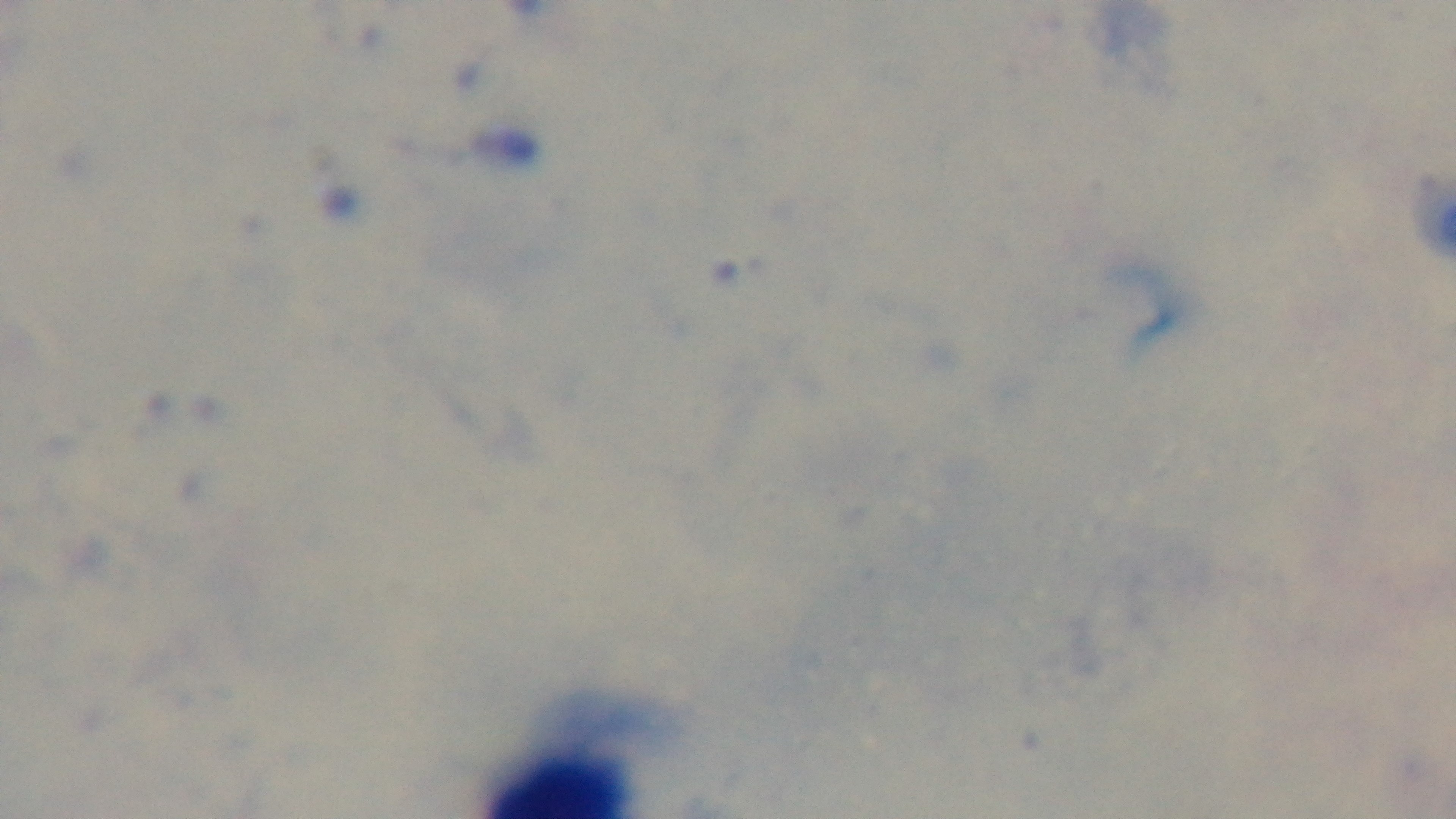
capture = mounted 4K digital camera
field of view = single
preparation = thick blood film
objective = 100x oil immersion
modality = light microscopy
stain = Giemsa
malaria status = uninfected